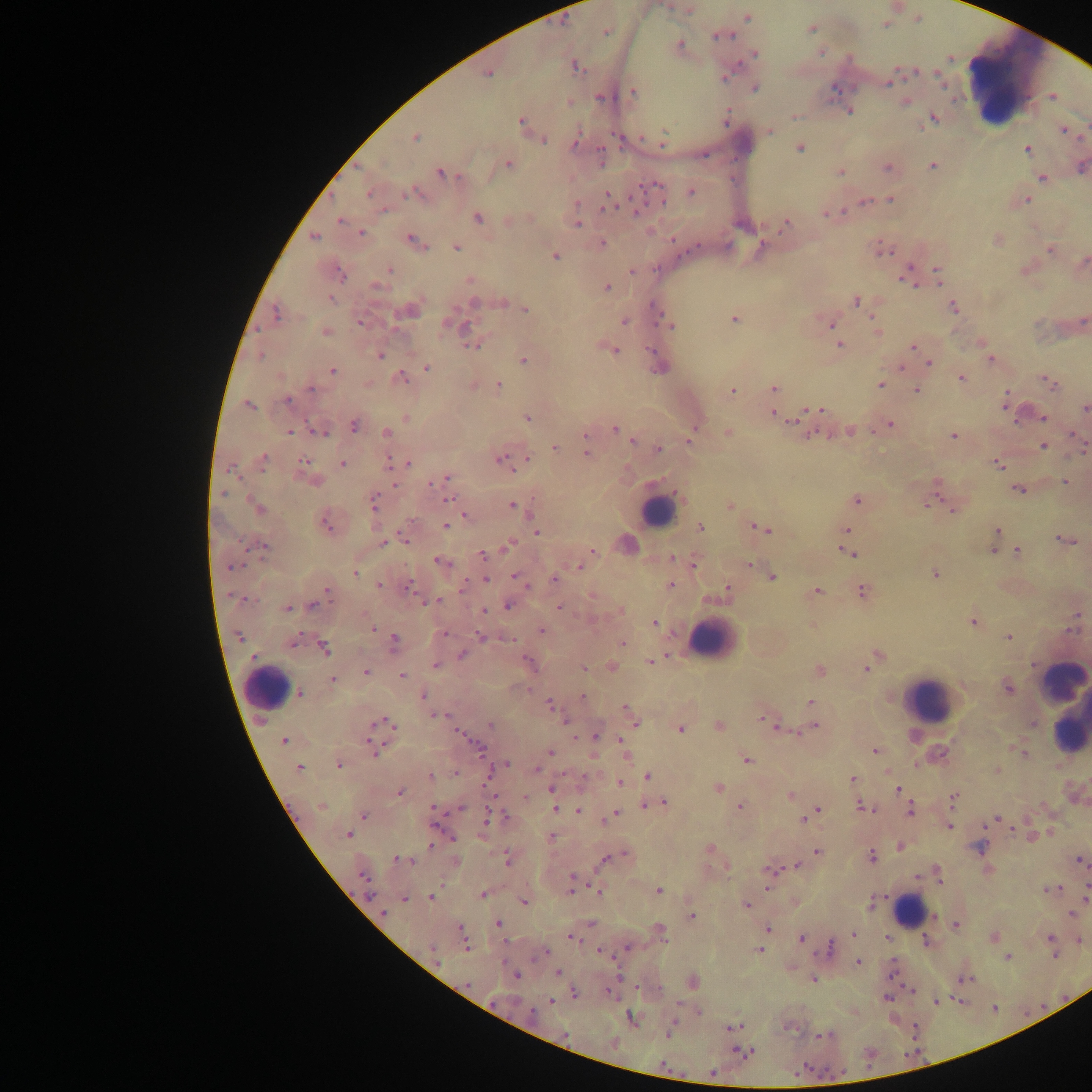

Approximate centers as [x, y] in pixels.
Summary:
  - Plasmodium parasite locations: [687, 11], [747, 17], [917, 19], [885, 23], [811, 28], [605, 31], [721, 35], [679, 46], [820, 51], [754, 53], [574, 66], [488, 72], [724, 75], [939, 75], [889, 80], [754, 87], [631, 91], [1053, 96], [905, 101], [848, 111], [794, 116], [726, 117], [933, 118], [521, 122], [769, 130], [1063, 130], [415, 137], [540, 138], [575, 141], [662, 142], [800, 148], [1027, 148], [602, 157], [508, 164], [932, 165], [1081, 166], [888, 167], [840, 172], [441, 173], [1042, 177], [415, 192], [691, 192], [369, 193], [608, 194], [889, 199], [1026, 199], [608, 202], [864, 202], [636, 211], [827, 213], [476, 217], [340, 220], [576, 223], [785, 224], [650, 231], [360, 233], [314, 237], [998, 239], [413, 240], [602, 244], [760, 246], [455, 247], [880, 249], [1050, 249], [553, 255], [1082, 262], [1025, 268], [632, 269], [389, 270], [907, 272], [338, 273], [937, 276], [469, 279], [377, 285], [606, 287], [329, 298], [855, 300], [501, 302], [513, 304], [953, 306], [410, 309], [524, 310], [275, 314], [733, 318], [624, 320], [360, 321], [831, 323], [670, 325], [325, 331], [877, 331], [980, 342], [472, 344], [839, 344], [912, 347], [614, 349], [380, 355], [989, 356], [522, 358], [992, 359], [929, 362], [900, 366], [426, 368], [332, 370], [961, 377], [400, 378], [1047, 381], [881, 384], [473, 385], [497, 385], [774, 387], [915, 390], [731, 391], [288, 400], [1005, 401], [249, 405], [1084, 408], [819, 410], [803, 412], [773, 413], [1044, 417], [406, 418], [527, 418], [354, 425], [889, 425], [694, 426], [318, 429], [614, 429], [290, 431], [848, 431], [386, 432], [727, 433], [586, 435], [953, 435], [633, 440], [690, 440], [585, 444], [1081, 444], [1043, 446], [555, 447], [657, 450], [586, 453], [527, 458], [263, 459], [501, 460], [304, 462], [389, 463], [408, 463], [997, 463], [342, 464], [445, 478], [314, 481], [1066, 481], [433, 482], [936, 487], [1018, 488], [447, 499], [856, 500], [931, 501], [373, 502], [511, 505], [257, 506], [730, 506], [952, 507], [519, 509], [465, 515], [326, 521], [446, 526], [700, 528], [761, 528], [844, 530], [997, 530], [536, 532], [404, 537], [1065, 539], [384, 542], [508, 545], [263, 546], [992, 549], [848, 550], [591, 551], [1017, 551], [483, 553], [672, 558], [586, 559], [441, 562], [693, 562], [748, 564], [579, 566], [355, 572], [934, 574], [518, 576], [771, 576], [485, 578], [555, 579], [379, 585], [408, 585], [671, 585], [727, 589], [816, 590], [863, 590], [325, 592], [592, 595], [316, 602], [429, 602], [508, 605], [559, 606], [287, 607], [482, 610], [619, 610], [1076, 617], [654, 622], [972, 622], [812, 625], [371, 627], [541, 630], [442, 634], [481, 635], [1008, 637], [293, 641], [393, 643], [622, 643], [324, 648], [462, 654], [877, 656], [650, 661], [529, 663], [870, 663], [435, 665], [610, 667], [583, 668], [819, 670], [365, 671], [402, 675], [332, 679], [1007, 686], [300, 693], [423, 696], [582, 696], [811, 702], [549, 706], [625, 708], [630, 713], [436, 715], [764, 719], [565, 720], [382, 722], [634, 722], [491, 724], [772, 724], [719, 725], [815, 726], [379, 729], [679, 729], [459, 732], [595, 736], [284, 741], [374, 748], [874, 750], [1021, 751], [550, 752], [625, 754], [745, 759], [339, 764], [503, 766], [299, 768], [536, 769], [430, 776], [647, 777], [852, 779], [620, 783], [717, 788], [551, 789], [897, 789], [400, 792], [790, 795], [525, 797], [954, 798], [660, 803], [650, 805], [322, 806], [740, 806], [864, 806], [433, 808], [554, 808], [909, 809], [578, 811], [813, 813], [362, 815], [614, 815], [807, 816], [997, 818], [949, 826], [348, 835], [551, 837], [1032, 837], [899, 846], [980, 848], [709, 849], [817, 851], [871, 856], [610, 857], [506, 858], [401, 860], [1080, 860], [455, 861], [798, 865], [771, 870], [938, 874], [366, 882], [572, 884], [1050, 889], [658, 890], [598, 891], [482, 894], [1086, 896], [431, 897], [405, 899], [523, 902], [870, 904], [745, 905], [382, 912], [1072, 914], [691, 916], [498, 924], [955, 924], [767, 928], [659, 931], [854, 934], [462, 936], [573, 937], [887, 937], [993, 937], [802, 939], [1050, 939], [1078, 939], [830, 948], [758, 950], [599, 951], [545, 952], [1007, 957], [858, 962], [557, 972], [514, 974], [965, 978], [813, 979], [692, 982], [574, 993], [551, 1001], [936, 1001], [632, 1019], [733, 1028], [744, 1053]
  - Leukocyte locations: [1009, 75], [657, 512], [625, 544], [712, 639], [265, 687], [1062, 701], [928, 702], [910, 911]
  - Capture: mobile-phone photograph through a microscope
  - Field of view: single
  - Country: Ghana
  - Preparation: thick blood smear
  - Image size: 1092×1092 pixels